Identify the cell.
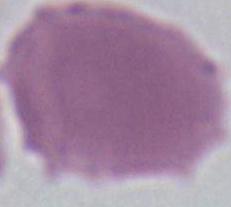

This is an erythrocyte.

magnification = 1000x
modality = micrograph